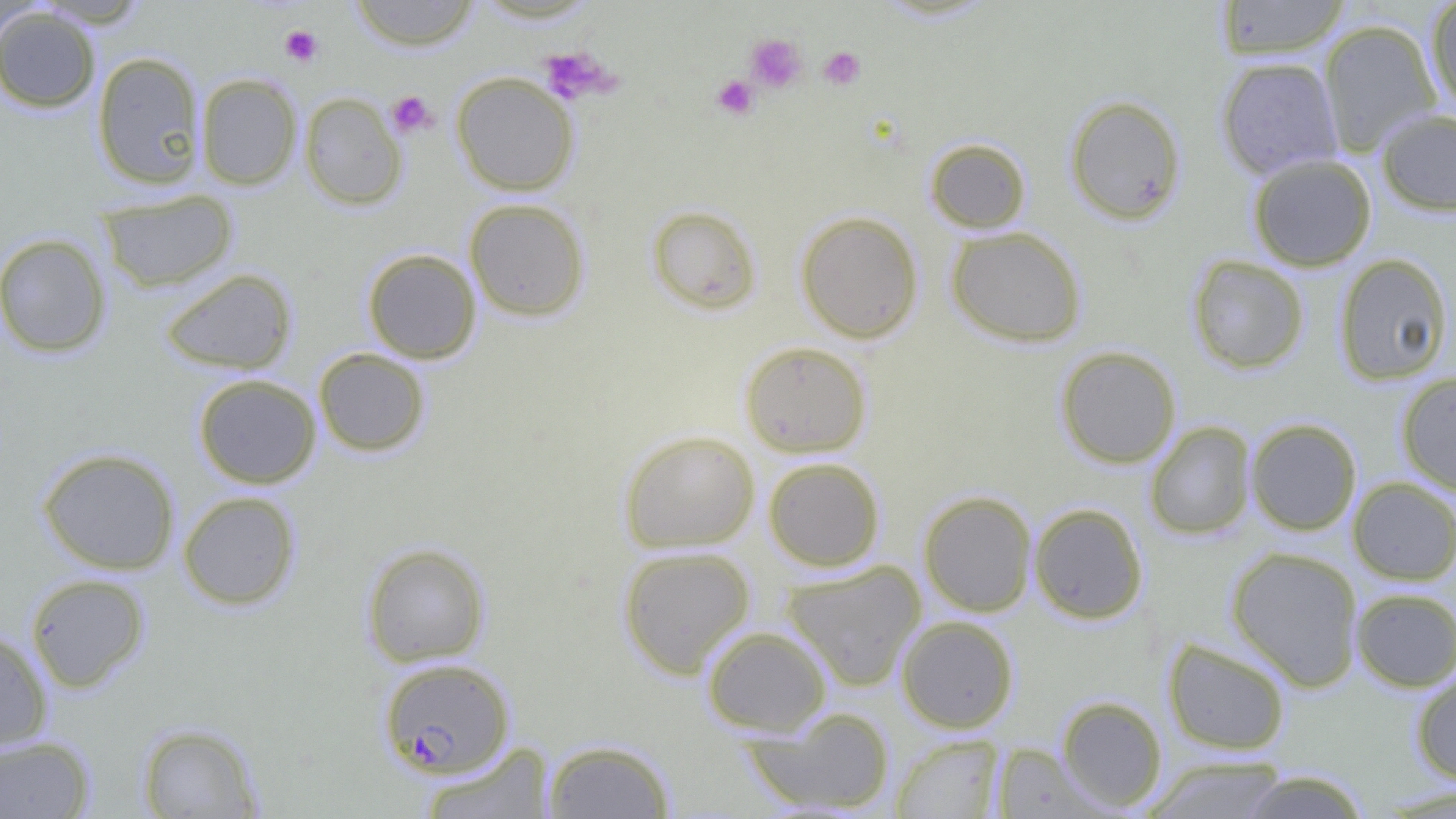

Approximate bounding boxes as (x1,y1)-(x2,y2) corner pairs in pixels. Platelet locations: (280,25)-(323,67), (744,32)-(807,93), (538,46)-(615,105), (818,46)-(866,90), (712,75)-(759,120), (386,91)-(436,137). Uninfected red blood cell locations: (349,0)-(481,51), (1214,0)-(1352,60), (1425,0)-(1456,113), (0,6)-(100,113), (1318,19)-(1442,156), (92,51)-(205,190), (1216,56)-(1343,179), (451,72)-(579,196), (195,73)-(302,190), (299,92)-(407,210), (1064,94)-(1187,225), (1376,109)-(1456,216), (924,137)-(1031,233), (1247,154)-(1377,272), (98,189)-(238,293), (464,198)-(590,322), (646,204)-(762,315), (795,210)-(923,343), (946,226)-(1087,347), (0,233)-(111,358), (362,248)-(481,363), (1334,253)-(1453,385), (1187,255)-(1310,374), (160,268)-(297,374), (739,340)-(872,458), (1055,346)-(1181,468), (313,348)-(431,457), (1395,371)-(1456,495), (193,374)-(321,489), (1246,418)-(1362,536), (1144,421)-(1256,541), (618,429)-(759,553), (37,447)-(180,574), (763,456)-(884,571), (1348,477)-(1456,585), (918,490)-(1037,617), (177,491)-(301,610), (1029,503)-(1148,624), (361,542)-(491,667), (617,545)-(755,679), (1226,546)-(1364,691), (781,561)-(926,692), (25,572)-(150,693), (1350,587)-(1456,692), (897,615)-(1019,733), (702,624)-(832,736), (0,626)-(53,752), (1162,637)-(1291,756), (1410,666)-(1456,785), (1056,695)-(1168,812), (741,706)-(896,814), (136,722)-(263,818), (0,734)-(95,818), (891,734)-(1005,818), (542,739)-(675,818), (419,741)-(556,818), (992,742)-(1108,818), (1140,756)-(1293,819), (1236,770)-(1373,818), (1376,784)-(1456,817). Plasmodium falciparum-infected red blood cell locations: (379,657)-(514,779). Slide-level diagnosis: Plasmodium falciparum. Captured at 1000x magnification. Image is 1456×819 pixels. Thin blood film. One field of a larger specimen. Light microscopy.